Give the position of every Plasmodium parasite.
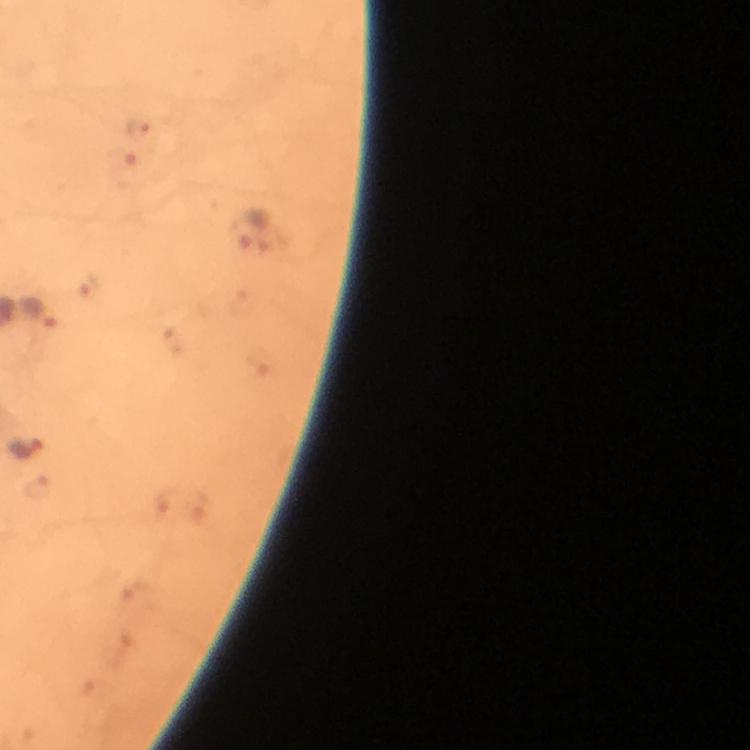

Approximate centers as {x, y} in pixels.
Plasmodium parasites: {139, 127}, {248, 230}, {41, 312}, {26, 447}.

image_size: 750×750 pixels
immersion_oil: applied
preparation: thick smear
stain: Giemsa
magnification: 100x
capture: smartphone camera through the microscope
cropped_from: one field of view
context: from a malaria diagnostic workup